Locate every blood parasite and identify its species.
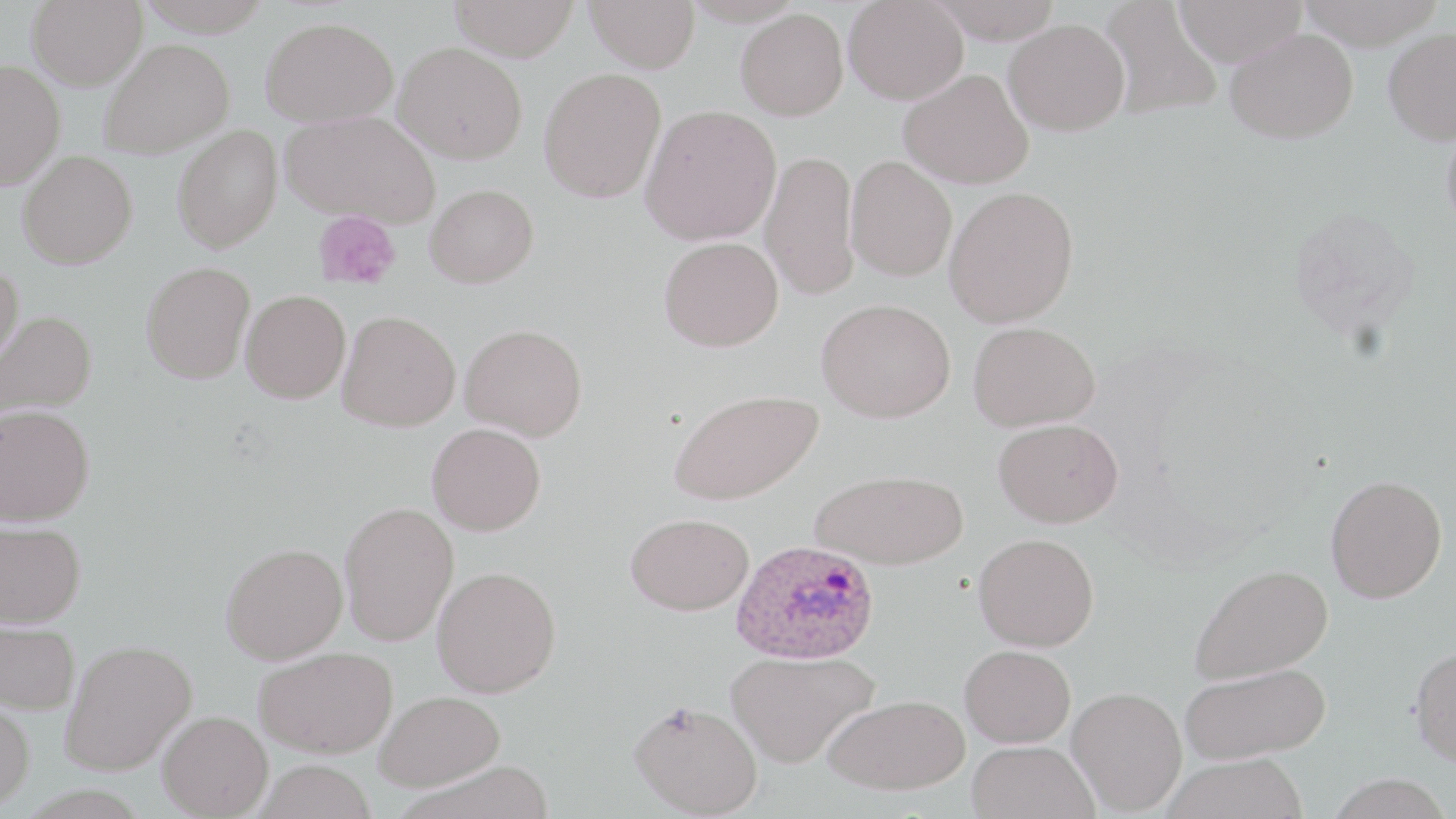
Approximate bounding boxes as [x1, y1, x2, y2] in pixels.
Plasmodium ovale-infected red blood cells: [731, 538, 881, 665].
No Plasmodium falciparum, Plasmodium malariae, Plasmodium vivax, Babesia divergens, or Trypanosoma brucei observed.

Uninfected red blood cell locations: [27, 0, 147, 90], [136, 0, 275, 37], [447, 0, 580, 62], [585, 0, 700, 73], [927, 0, 1065, 44], [1099, 0, 1221, 121], [1173, 0, 1308, 66], [1297, 0, 1447, 50], [843, 1, 968, 105], [735, 8, 848, 120], [261, 16, 398, 128], [1004, 19, 1130, 135], [1225, 28, 1358, 144], [1383, 28, 1456, 145], [99, 38, 234, 159], [394, 42, 528, 164], [0, 59, 65, 189], [538, 67, 667, 203], [898, 68, 1034, 189], [640, 104, 781, 245], [281, 111, 441, 228], [1440, 117, 1456, 239], [172, 125, 283, 253], [760, 149, 859, 301], [18, 150, 138, 269], [845, 156, 957, 281], [425, 183, 539, 288], [944, 185, 1079, 328], [659, 236, 784, 352], [0, 261, 24, 375], [141, 261, 255, 384], [240, 289, 351, 403], [816, 298, 956, 423], [0, 310, 97, 424], [338, 310, 461, 431], [968, 321, 1100, 432], [460, 323, 588, 441], [668, 388, 823, 505], [0, 404, 94, 526], [993, 417, 1123, 527], [426, 423, 546, 535], [810, 469, 968, 570], [1325, 474, 1447, 603], [339, 501, 459, 647], [625, 512, 753, 615], [0, 520, 86, 627], [973, 533, 1099, 651], [221, 542, 347, 664], [1190, 563, 1333, 684], [432, 566, 561, 697], [0, 617, 80, 714], [60, 639, 197, 775], [959, 644, 1076, 747], [1409, 645, 1456, 766], [253, 646, 397, 757], [726, 649, 879, 768], [1179, 662, 1332, 764], [1067, 686, 1187, 814], [375, 690, 505, 791], [823, 693, 971, 795], [0, 698, 35, 812], [629, 699, 763, 817], [157, 710, 273, 818], [967, 740, 1098, 819], [1161, 753, 1309, 819], [395, 758, 559, 818], [253, 759, 378, 819]. Platelet locations: [313, 211, 402, 290]. Slide-level diagnosis: Plasmodium ovale. Captured at 1000x magnification. Single field of view. Thin blood smear. Optical microscopy. Image is 1456×819 pixels. May-Grünwald-Giemsa stain.